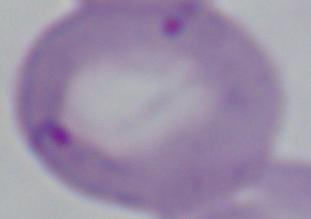

A Babesia parasite is shown. Captured at 1000x magnification. Photomicrograph.